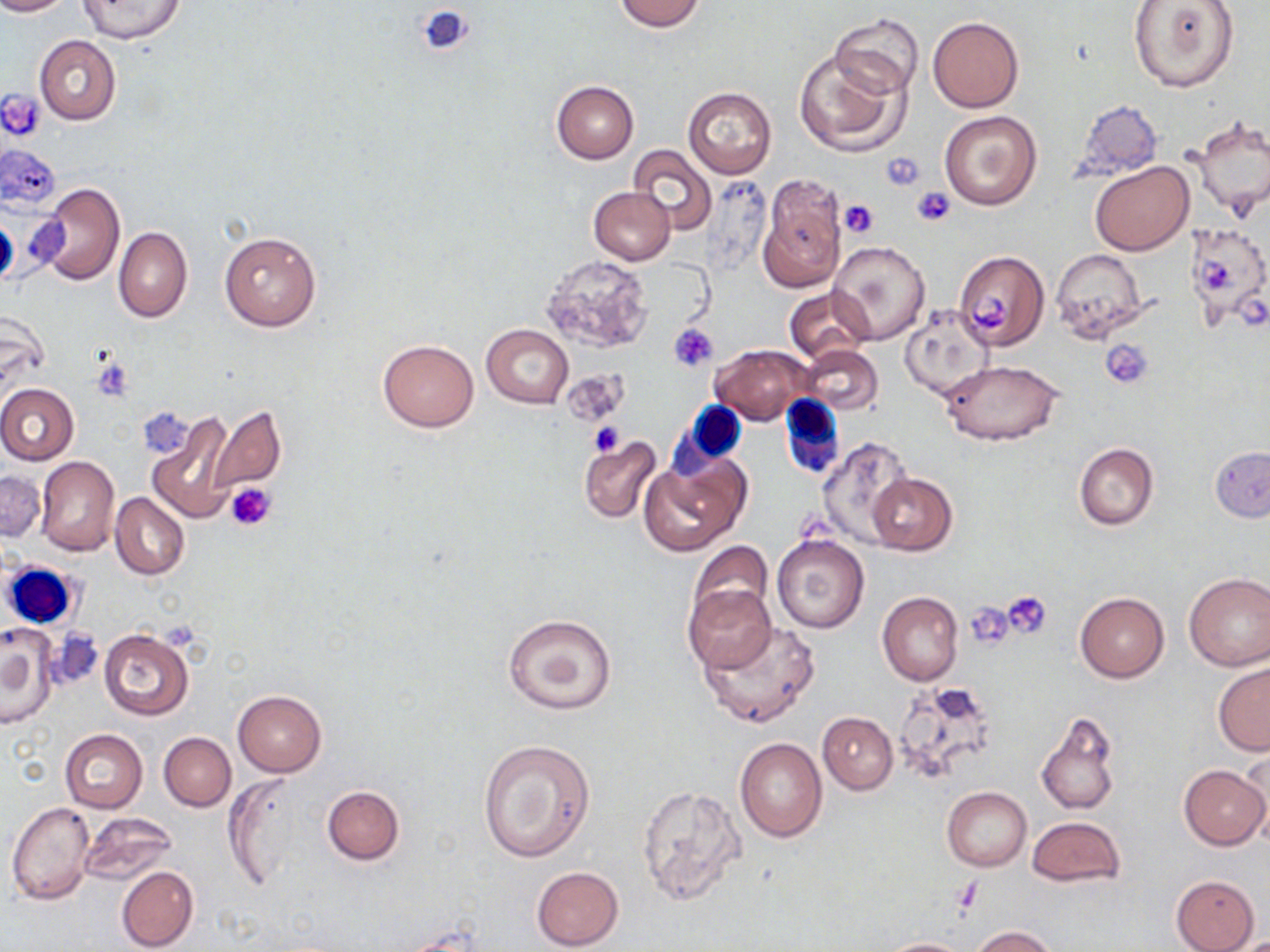
Summary:
  - Coordinate format: approximate bounding boxes as [x1, y1, x2, y2] in pixels
  - Platelet locations: [418, 3, 474, 57], [1, 90, 43, 141], [879, 152, 925, 192], [911, 187, 956, 226], [839, 199, 879, 239], [1199, 256, 1236, 292], [969, 290, 1015, 332], [671, 323, 718, 370], [1101, 337, 1154, 388], [92, 356, 136, 402], [574, 380, 626, 433], [589, 422, 625, 455], [225, 482, 276, 532], [1002, 591, 1053, 638], [965, 601, 1017, 648], [949, 880, 984, 915]
  - White blood cell locations: [779, 394, 845, 480], [678, 399, 749, 469], [3, 560, 81, 632]
  - Uninfected red blood cell locations: [0, 0, 75, 16], [77, 0, 187, 44], [612, 0, 706, 31], [1128, 0, 1240, 94], [830, 13, 923, 98], [928, 16, 1024, 113], [34, 35, 121, 125], [794, 46, 910, 157], [551, 80, 639, 163], [683, 86, 776, 179], [1073, 100, 1163, 183], [939, 111, 1043, 211], [1187, 113, 1270, 219], [1, 142, 60, 212], [628, 145, 716, 235], [1090, 161, 1193, 255], [758, 175, 846, 292], [705, 178, 774, 277], [36, 182, 124, 286], [589, 186, 675, 265], [114, 227, 192, 322], [1183, 228, 1267, 321], [219, 232, 322, 331], [830, 241, 928, 344], [1050, 248, 1150, 340], [955, 249, 1048, 352], [540, 254, 653, 353], [784, 287, 874, 365], [899, 308, 994, 400], [0, 309, 50, 401], [480, 324, 573, 408], [378, 338, 479, 432], [711, 344, 811, 425], [798, 344, 883, 414], [941, 361, 1064, 447], [561, 372, 629, 425], [0, 383, 78, 465], [207, 406, 286, 493], [146, 412, 238, 522], [577, 435, 662, 523], [816, 435, 915, 546], [1074, 442, 1159, 530], [1210, 446, 1270, 522], [35, 456, 119, 556], [640, 456, 747, 558], [0, 471, 46, 543], [866, 471, 958, 555], [110, 493, 189, 579], [771, 533, 870, 633], [687, 542, 774, 625], [1183, 572, 1270, 671], [682, 585, 775, 674], [877, 590, 963, 686], [1074, 592, 1169, 682], [503, 614, 618, 715], [698, 619, 823, 729], [39, 624, 105, 698], [0, 627, 56, 729], [99, 628, 195, 722], [1213, 662, 1270, 756], [891, 681, 998, 786], [233, 690, 327, 777], [1036, 710, 1120, 816], [817, 712, 897, 793], [60, 728, 148, 813], [159, 732, 236, 811], [735, 737, 828, 842], [478, 739, 593, 862], [1181, 764, 1269, 849], [223, 777, 302, 890], [636, 784, 747, 908], [322, 785, 404, 864], [943, 786, 1031, 871], [6, 802, 96, 906], [78, 811, 177, 887], [1027, 817, 1124, 888], [115, 866, 198, 952], [531, 866, 623, 950], [1171, 875, 1260, 952], [970, 925, 1058, 951], [878, 937, 974, 952]
  - Slide-level diagnosis: no evidence of blood parasites
  - Image size: 1270×952 pixels
  - Stain: May-Grünwald-Giemsa
  - Magnification: 1000x
  - Modality: light microscopy
  - Field of view: single
  - Preparation: thin blood smear